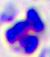

{
  "identification": "white blood cell",
  "modality": "photomicrograph",
  "magnification": "400x"
}